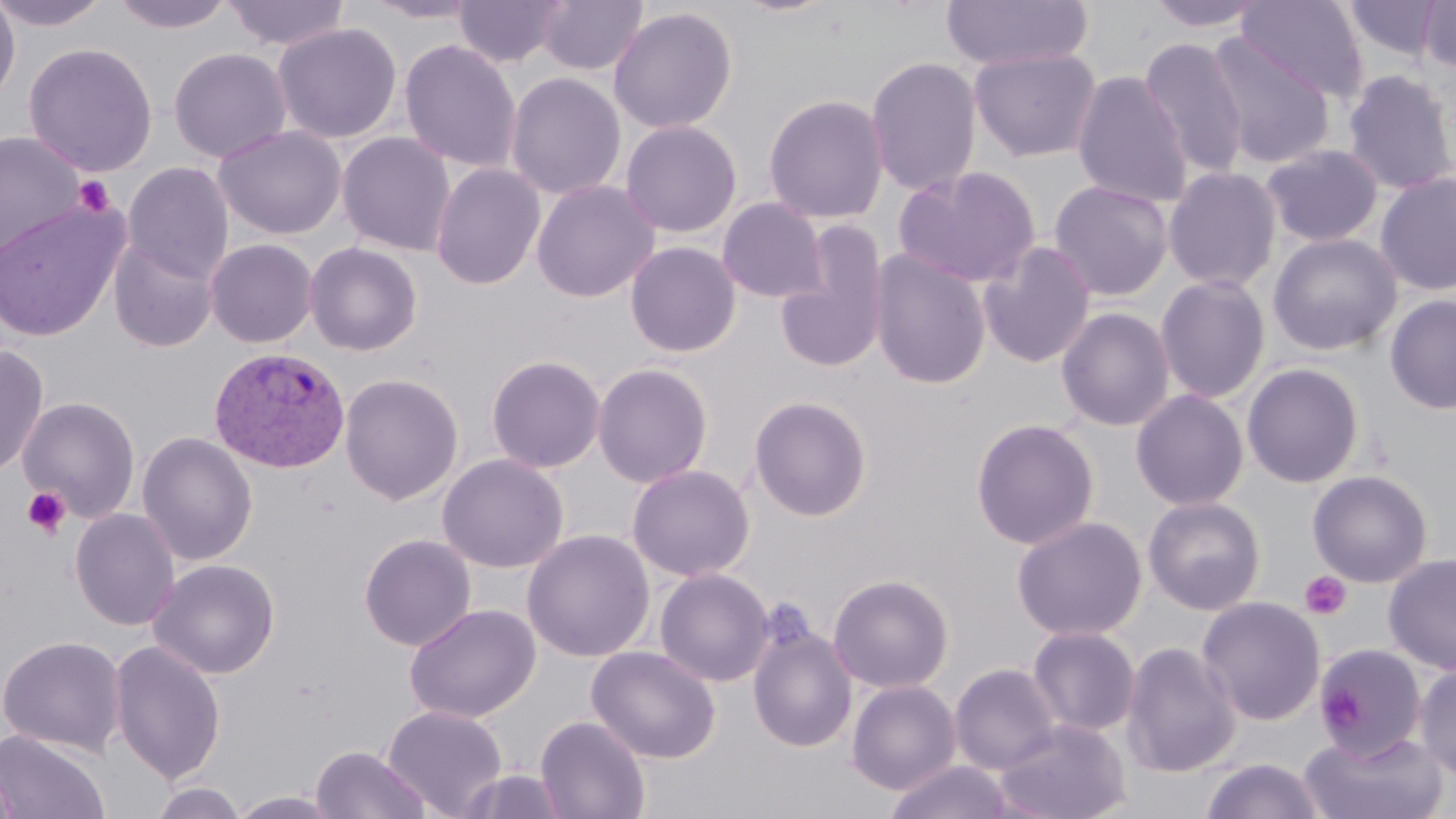

slide-level diagnosis = Plasmodium vivax
stain = May-Grünwald-Giemsa
modality = light microscopy
image size = 1456×819 pixels
preparation = thin blood smear
uninfected red blood cell locations = approximate bounding boxes as named x1/y1/x2/y2 corners in pixels: (x1=0, y1=0, x2=112, y2=31), (x1=109, y1=0, x2=237, y2=34), (x1=221, y1=0, x2=351, y2=52), (x1=362, y1=0, x2=483, y2=24), (x1=454, y1=0, x2=566, y2=69), (x1=537, y1=0, x2=648, y2=77), (x1=940, y1=0, x2=1093, y2=72), (x1=1142, y1=0, x2=1269, y2=33), (x1=1342, y1=0, x2=1447, y2=64), (x1=0, y1=1, x2=21, y2=108), (x1=1236, y1=1, x2=1370, y2=103), (x1=1416, y1=1, x2=1456, y2=75), (x1=608, y1=6, x2=738, y2=135), (x1=272, y1=22, x2=402, y2=143), (x1=1203, y1=32, x2=1336, y2=171), (x1=1139, y1=36, x2=1249, y2=182), (x1=398, y1=38, x2=522, y2=173), (x1=23, y1=41, x2=158, y2=177), (x1=168, y1=47, x2=292, y2=163), (x1=968, y1=47, x2=1102, y2=163), (x1=866, y1=55, x2=982, y2=197), (x1=1342, y1=69, x2=1456, y2=195), (x1=1071, y1=70, x2=1192, y2=208), (x1=504, y1=71, x2=627, y2=200), (x1=763, y1=93, x2=889, y2=224), (x1=620, y1=119, x2=743, y2=238), (x1=213, y1=125, x2=347, y2=240), (x1=0, y1=130, x2=86, y2=260), (x1=336, y1=132, x2=456, y2=257), (x1=1260, y1=143, x2=1385, y2=247), (x1=123, y1=162, x2=234, y2=283), (x1=430, y1=162, x2=546, y2=290), (x1=893, y1=165, x2=1041, y2=289), (x1=1163, y1=165, x2=1283, y2=293), (x1=1374, y1=171, x2=1456, y2=296), (x1=530, y1=179, x2=659, y2=303), (x1=1049, y1=180, x2=1174, y2=301), (x1=716, y1=198, x2=827, y2=304), (x1=0, y1=199, x2=129, y2=342), (x1=775, y1=222, x2=891, y2=376), (x1=1268, y1=233, x2=1402, y2=356), (x1=109, y1=236, x2=221, y2=353), (x1=205, y1=238, x2=318, y2=348), (x1=625, y1=241, x2=741, y2=358), (x1=979, y1=241, x2=1097, y2=368), (x1=304, y1=242, x2=423, y2=356), (x1=869, y1=249, x2=992, y2=389), (x1=1155, y1=275, x2=1271, y2=404), (x1=1384, y1=295, x2=1456, y2=415), (x1=1056, y1=307, x2=1175, y2=432), (x1=0, y1=344, x2=49, y2=480), (x1=486, y1=354, x2=606, y2=473), (x1=593, y1=362, x2=713, y2=488), (x1=1242, y1=363, x2=1364, y2=488), (x1=340, y1=372, x2=464, y2=506), (x1=1130, y1=389, x2=1249, y2=511), (x1=749, y1=395, x2=872, y2=521), (x1=18, y1=396, x2=141, y2=522), (x1=970, y1=418, x2=1100, y2=550), (x1=137, y1=431, x2=258, y2=565), (x1=437, y1=453, x2=569, y2=573), (x1=627, y1=463, x2=755, y2=582), (x1=1307, y1=469, x2=1433, y2=588), (x1=1142, y1=495, x2=1266, y2=615), (x1=69, y1=508, x2=180, y2=631), (x1=1011, y1=515, x2=1147, y2=641), (x1=521, y1=529, x2=656, y2=662), (x1=358, y1=533, x2=477, y2=651), (x1=1382, y1=553, x2=1456, y2=676), (x1=147, y1=558, x2=281, y2=680), (x1=654, y1=568, x2=773, y2=686), (x1=828, y1=573, x2=954, y2=693), (x1=1197, y1=596, x2=1325, y2=726), (x1=404, y1=604, x2=541, y2=724), (x1=748, y1=624, x2=858, y2=753), (x1=1027, y1=626, x2=1140, y2=737), (x1=0, y1=635, x2=126, y2=756), (x1=109, y1=639, x2=226, y2=783), (x1=1120, y1=640, x2=1241, y2=778), (x1=586, y1=645, x2=721, y2=763), (x1=1314, y1=645, x2=1426, y2=762), (x1=949, y1=663, x2=1060, y2=775), (x1=1414, y1=663, x2=1456, y2=781), (x1=846, y1=679, x2=961, y2=795), (x1=382, y1=705, x2=508, y2=818), (x1=535, y1=714, x2=651, y2=819), (x1=992, y1=717, x2=1132, y2=819), (x1=0, y1=729, x2=111, y2=819), (x1=1298, y1=730, x2=1450, y2=819), (x1=310, y1=745, x2=432, y2=819), (x1=1199, y1=758, x2=1327, y2=819), (x1=884, y1=759, x2=1018, y2=819), (x1=0, y1=763, x2=22, y2=819), (x1=456, y1=768, x2=570, y2=818), (x1=148, y1=781, x2=248, y2=819), (x1=228, y1=791, x2=344, y2=818)
magnification = 1000x
field of view = single
platelet locations = approximate bounding boxes as named x1/y1/x2/y2 corners in pixels: (x1=74, y1=174, x2=115, y2=216), (x1=21, y1=487, x2=71, y2=539), (x1=1300, y1=571, x2=1352, y2=621), (x1=1318, y1=681, x2=1361, y2=732)
Plasmodium vivax-infected red blood cell locations = approximate bounding boxes as named x1/y1/x2/y2 corners in pixels: (x1=208, y1=346, x2=351, y2=473)